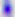

magnification = 400x
modality = photomicrograph
identification = Toxoplasma gondii